Report the malaria status of this cell.
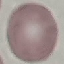
Uninfected.

Summary:
  - Preparation: thin smear
  - Capture: smartphone camera at the microscope eyepiece
  - Stain: Giemsa
  - Image type: automatically extracted cell patch, resized to 64 × 64 pixels